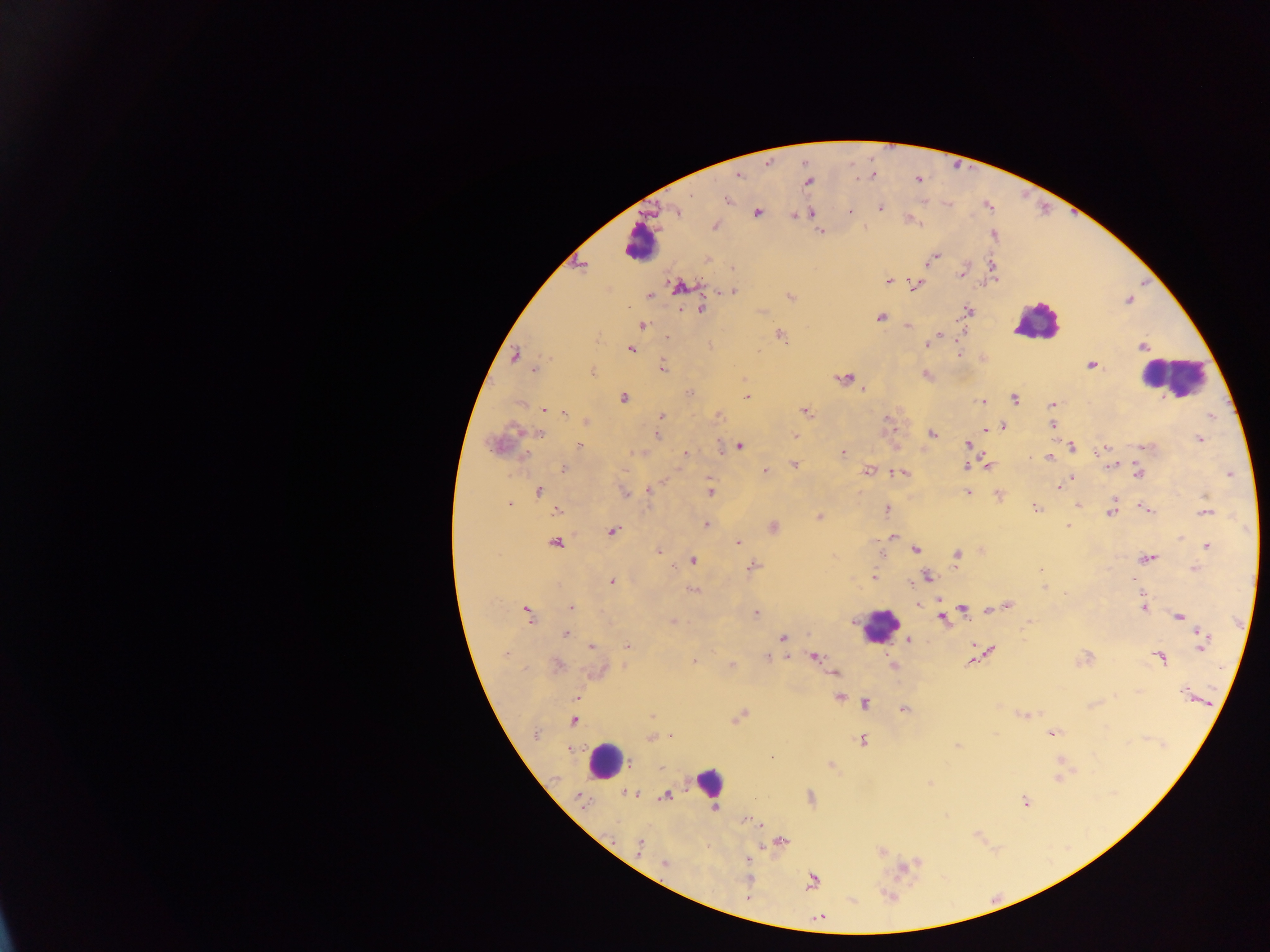
{
  "plasmodium_parasite_locations": "approximate centers as x y in pixels: 738 175; 918 179; 808 181; 727 199; 880 208; 676 211; 849 211; 757 213; 811 213; 795 216; 715 226; 820 232; 934 257; 582 265; 734 269; 962 273; 890 281; 915 285; 681 287; 731 292; 649 296; 790 296; 701 309; 968 310; 880 317; 642 326; 907 326; 941 334; 779 335; 666 337; 926 345; 1142 346; 631 350; 959 354; 515 356; 1091 365; 662 366; 535 369; 593 371; 926 374; 843 379; 863 389; 691 393; 747 397; 623 398; 1014 398; 981 402; 1053 404; 544 410; 805 412; 565 413; 662 415; 718 416; 587 422; 1052 425; 1003 427; 986 429; 538 434; 656 434; 932 434; 795 436; 1200 439; 967 444; 495 445; 580 445; 739 446; 1071 446; 1102 450; 637 452; 684 453; 843 453; 1049 458; 794 464; 1112 465; 966 466; 986 466; 564 469; 765 471; 868 471; 903 473; 1139 473; 1230 474; 1072 478; 1058 487; 538 491; 649 491; 711 492; 625 493; 969 493; 998 494; 1078 504; 509 506; 1035 507; 1145 508; 886 510; 557 511; 1111 512; 1205 513; 819 516; 707 524; 1067 526; 773 527; 612 531; 893 537; 556 542; 737 542; 1206 546; 916 549; 659 551; 958 555; 1148 559; 693 561; 753 566; 1194 569; 1041 570; 927 577; 873 578; 612 581; 1044 587; 692 590; 938 600; 918 604; 1008 606; 571 608; 963 609; 998 609; 1144 609; 527 613; 756 613; 941 617; 1179 617; 672 621; 1029 621; 565 634; 783 638; 908 641; 1202 641; 592 646; 627 646; 989 649; 506 654; 767 657; 789 657; 815 657; 1160 658; 694 660; 971 662; 557 666; 732 666; 600 671; 834 673; 1138 691; 1185 692; 576 698; 839 698; 865 704; 904 709; 1024 714; 652 715; 739 716; 573 721; 536 733; 1053 734; 670 736; 650 738; 862 741; 956 746; 1060 762; 830 764; 1058 778; 630 794; 666 796; 580 798; 1026 801; 746 819; 754 822; 781 841; 639 846; 749 859; 665 863; 903 867; 747 879; 812 881; 748 898; 820 918",
  "country": "Ghana",
  "image_size": "1270×952 pixels",
  "capture": "mobile-phone photograph through a microscope",
  "leukocyte_locations": "approximate centers as x y in pixels: 639 244; 1036 322; 1172 376; 879 625; 606 760; 708 782",
  "preparation": "thick blood film",
  "field_of_view": "single"
}